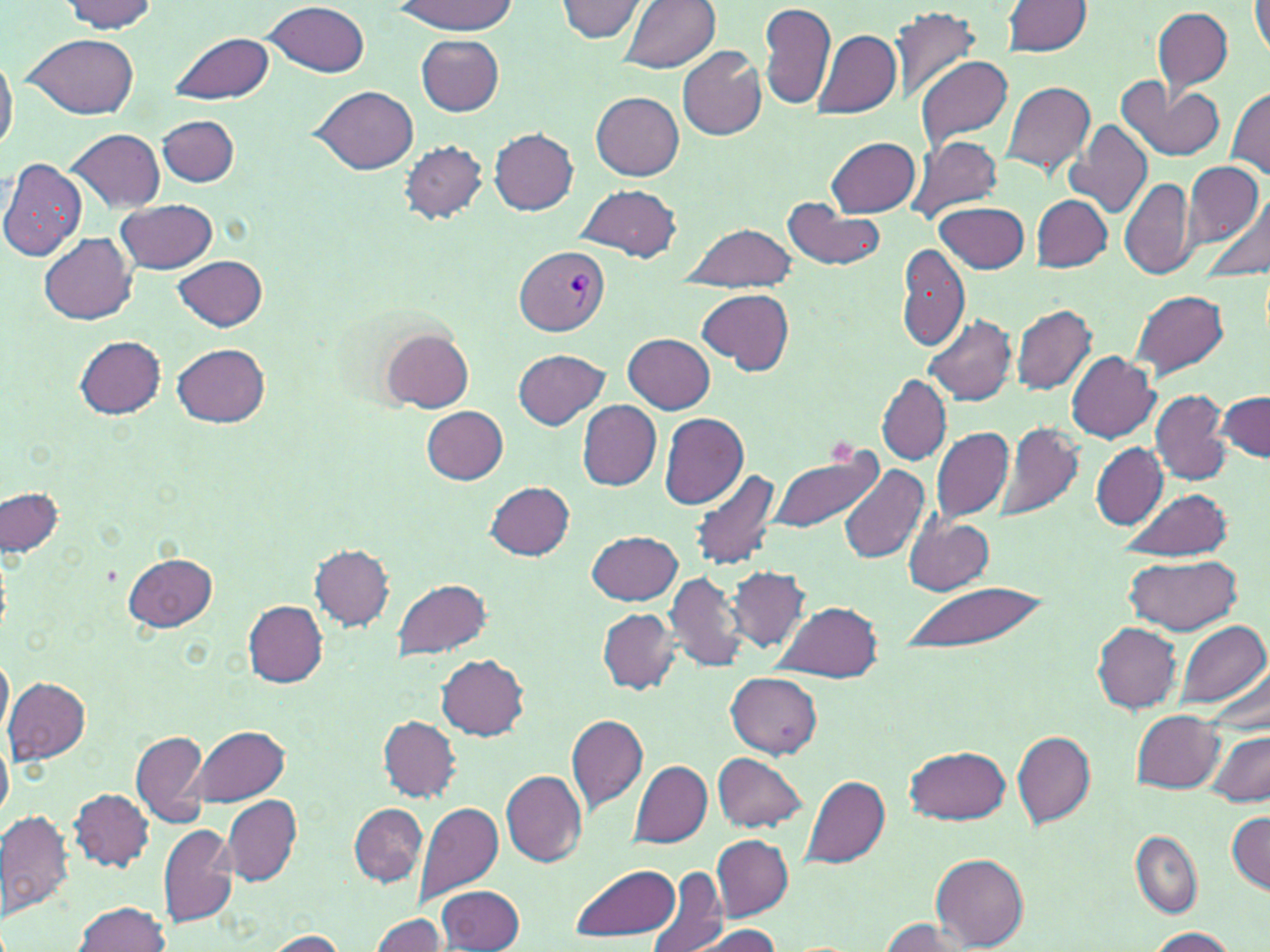 Approximate bounding boxes as (x1, y1, x2, y2) in pixels. Plasmodium vivax-infected red blood cell locations: (517, 246, 609, 335). Uninfected red blood cell locations: (392, 0, 519, 35), (557, 0, 646, 42), (59, 1, 158, 34), (263, 1, 368, 76), (616, 1, 719, 74), (1005, 1, 1091, 54), (1251, 2, 1270, 58), (759, 5, 836, 110), (889, 7, 981, 103), (1153, 7, 1233, 95), (811, 29, 900, 118), (169, 32, 274, 104), (24, 33, 139, 118), (416, 35, 503, 116), (677, 47, 766, 140), (0, 48, 17, 157), (915, 57, 1014, 151), (1117, 76, 1225, 162), (999, 81, 1094, 176), (311, 85, 418, 174), (1228, 88, 1270, 177), (592, 92, 684, 180), (157, 115, 240, 186), (1063, 118, 1153, 219), (490, 127, 578, 214), (68, 129, 164, 212), (906, 134, 1003, 225), (826, 137, 920, 217), (400, 141, 487, 222), (0, 157, 87, 261), (1184, 160, 1267, 255), (1119, 177, 1196, 279), (574, 185, 681, 261), (1198, 195, 1270, 283), (783, 196, 887, 271), (1032, 196, 1113, 271), (116, 198, 218, 275), (937, 201, 1029, 274), (680, 222, 797, 291), (41, 233, 136, 324), (896, 243, 969, 351), (174, 254, 267, 330), (1128, 288, 1229, 382), (698, 289, 793, 373), (1011, 304, 1096, 395), (923, 314, 1017, 405), (381, 329, 474, 412), (624, 334, 715, 413), (74, 336, 166, 419), (172, 343, 270, 427), (514, 348, 608, 429), (1066, 352, 1159, 442), (878, 377, 951, 464), (1151, 390, 1231, 485), (1216, 391, 1269, 463), (578, 401, 661, 490), (422, 406, 509, 483), (658, 412, 748, 510), (996, 421, 1082, 524), (932, 426, 1013, 521), (1091, 442, 1166, 529), (767, 446, 882, 535), (839, 465, 930, 564), (689, 469, 780, 570), (485, 481, 574, 559), (1121, 485, 1233, 562), (1, 487, 64, 558), (902, 516, 993, 595), (587, 530, 682, 605), (311, 544, 394, 629), (122, 552, 217, 632), (1127, 553, 1241, 636), (727, 567, 810, 652), (665, 571, 752, 673), (393, 578, 493, 660), (896, 579, 1050, 659), (773, 599, 884, 682), (242, 600, 328, 686), (597, 608, 680, 693), (1177, 619, 1269, 707), (1093, 622, 1182, 713), (0, 648, 13, 748), (436, 654, 528, 739), (726, 672, 822, 757), (3, 676, 90, 763), (1132, 709, 1223, 793), (567, 714, 648, 813), (379, 716, 461, 800), (189, 724, 291, 807), (131, 730, 211, 830), (1011, 731, 1094, 829), (1204, 731, 1268, 806), (0, 742, 11, 819), (904, 745, 1010, 826), (712, 752, 806, 830), (629, 760, 712, 847), (501, 769, 587, 867), (802, 775, 890, 867), (70, 788, 153, 871), (221, 795, 301, 884), (414, 802, 503, 906), (349, 804, 427, 887), (0, 810, 73, 922), (1227, 811, 1270, 890), (157, 822, 240, 929), (1131, 831, 1201, 919), (711, 834, 793, 921), (932, 852, 1028, 948), (569, 862, 681, 940), (646, 871, 728, 952), (437, 883, 525, 950), (74, 900, 170, 952), (369, 913, 448, 952), (879, 918, 978, 952), (690, 924, 785, 952), (1146, 927, 1236, 951), (264, 930, 348, 950). Slide-level diagnosis: Plasmodium vivax. Light microscopy. One field of a larger specimen. 1000x magnification. Image is 1270×952 pixels. Thin blood smear. May-Grünwald-Giemsa stain.